Assess the morphology of the red blood cells.
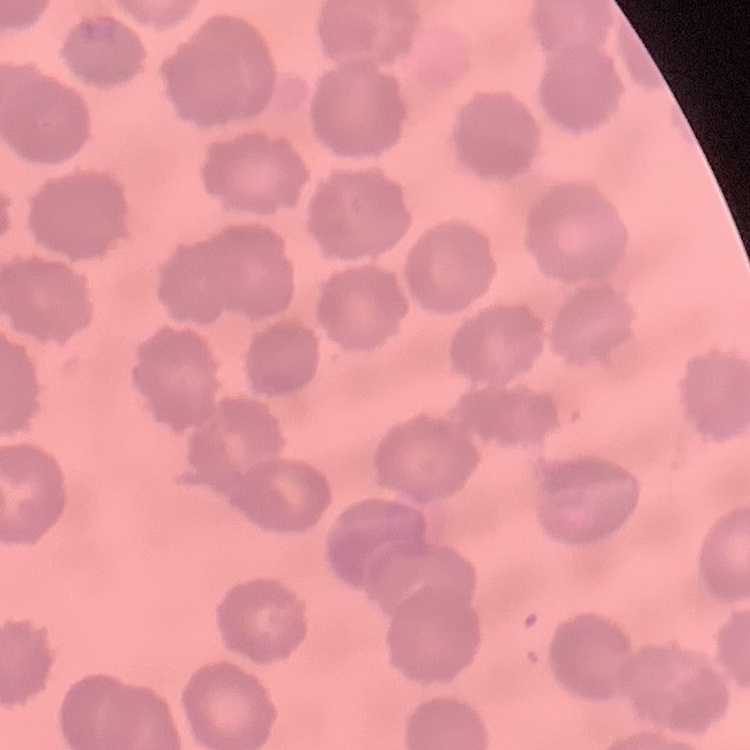
No rouleaux formation.

Thin blood film. Square crop of a larger photomicrograph. Field's or Giemsa stain.